Comment on the morphology of the erythrocytes.
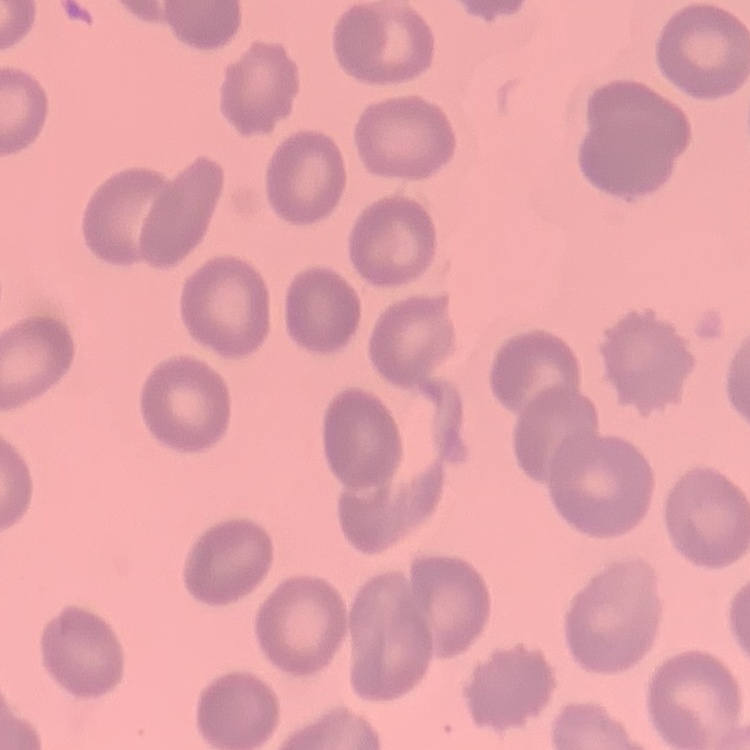
They show no rouleaux formation.

Summary:
  - Image type: one tile cut from a larger photomicrograph
  - Preparation: thin blood film
  - Stain: Field's or Giemsa